Name the parasite shown.
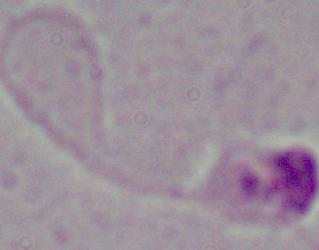

Leishmania.

magnification: 1000x
modality: micrograph